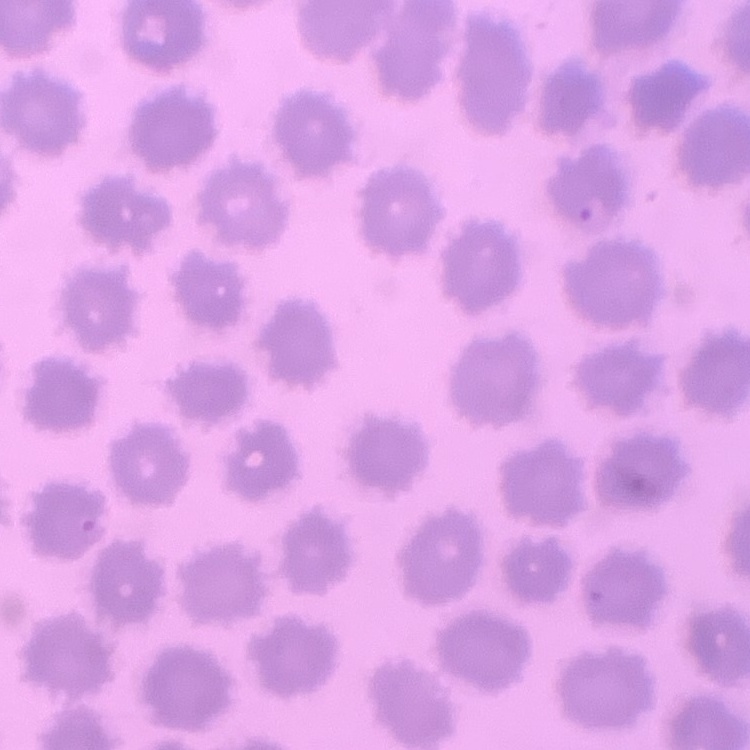

Summary:
  - Erythrocyte morphology: no rouleaux formation
  - Image type: square crop of a larger photomicrograph
  - Stain: Field's or Giemsa
  - Preparation: thin blood film